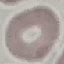
Result: negative for malaria parasites. Cell patch, automatically extracted from a larger field of view and resized to 64 × 64 pixels. Giemsa-stained preparation. Photographed with a smartphone camera at the microscope eyepiece. Thin smear of blood.